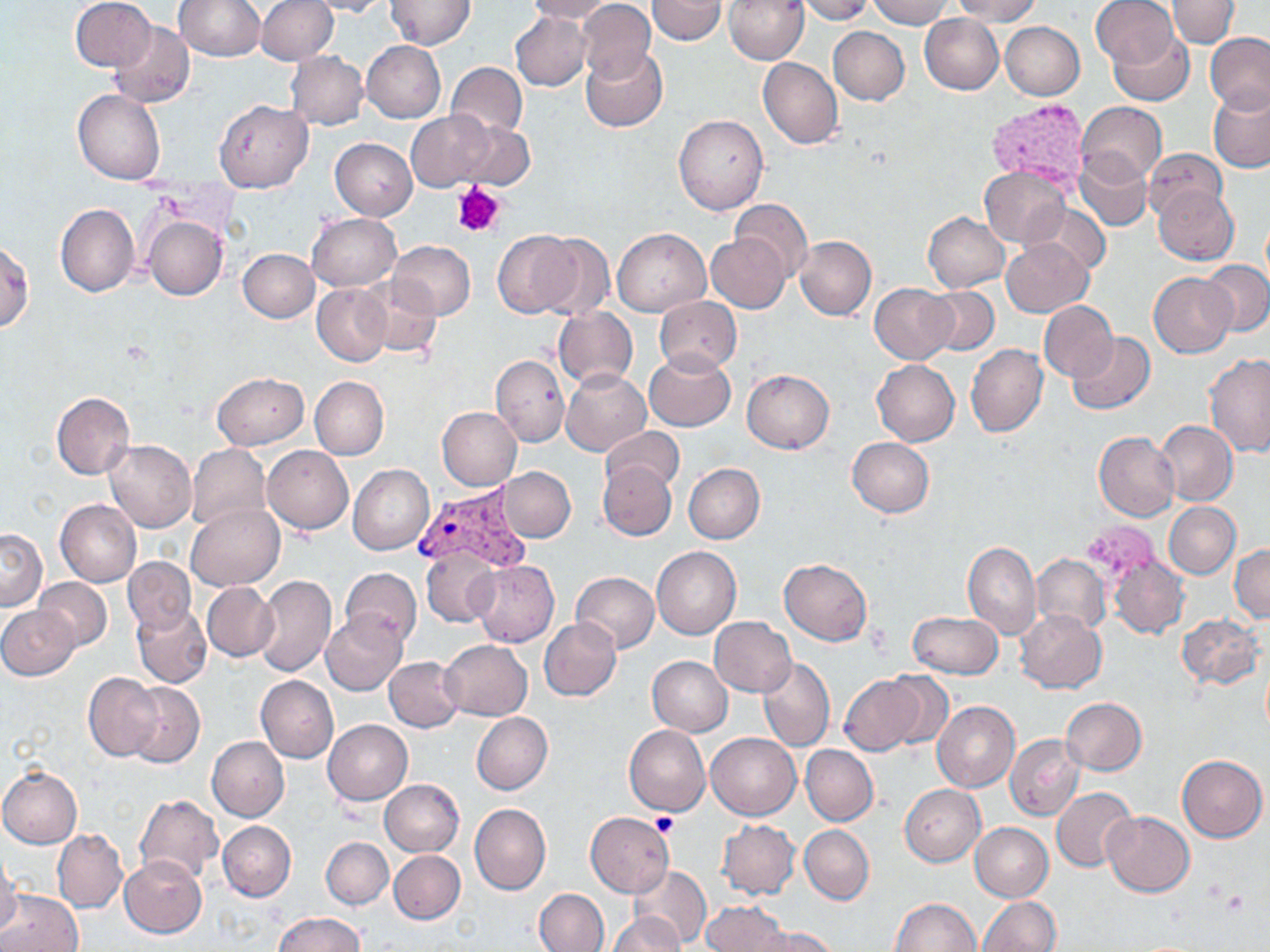

slide-level diagnosis = Plasmodium vivax
stain = May-Grünwald-Giemsa
modality = light microscopy
magnification = 1000x
image size = 1270×952 pixels
preparation = thin blood film
platelet locations = approximate bounding boxes as named x1/y1/x2/y2 corners in pixels: (x1=452, y1=181, x2=505, y2=239), (x1=651, y1=812, x2=676, y2=834)
uninfected red blood cell locations = approximate bounding boxes as named x1/y1/x2/y2 corners in pixels: (x1=71, y1=0, x2=157, y2=72), (x1=174, y1=0, x2=264, y2=61), (x1=256, y1=0, x2=338, y2=64), (x1=306, y1=0, x2=392, y2=17), (x1=385, y1=0, x2=476, y2=50), (x1=524, y1=0, x2=614, y2=23), (x1=576, y1=0, x2=655, y2=84), (x1=649, y1=0, x2=726, y2=46), (x1=796, y1=0, x2=874, y2=24), (x1=868, y1=0, x2=952, y2=26), (x1=950, y1=0, x2=1041, y2=25), (x1=1090, y1=0, x2=1180, y2=68), (x1=1167, y1=0, x2=1239, y2=48), (x1=723, y1=1, x2=808, y2=64), (x1=512, y1=13, x2=592, y2=90), (x1=919, y1=14, x2=1003, y2=94), (x1=108, y1=21, x2=195, y2=109), (x1=1001, y1=22, x2=1084, y2=99), (x1=828, y1=27, x2=909, y2=105), (x1=1107, y1=29, x2=1195, y2=107), (x1=1205, y1=32, x2=1270, y2=115), (x1=362, y1=40, x2=446, y2=123), (x1=581, y1=46, x2=667, y2=132), (x1=286, y1=52, x2=369, y2=129), (x1=757, y1=57, x2=842, y2=149), (x1=445, y1=61, x2=530, y2=140), (x1=72, y1=89, x2=166, y2=184), (x1=1208, y1=89, x2=1270, y2=172), (x1=214, y1=100, x2=313, y2=191), (x1=1076, y1=102, x2=1167, y2=186), (x1=405, y1=109, x2=501, y2=191), (x1=673, y1=113, x2=769, y2=215), (x1=451, y1=119, x2=537, y2=189), (x1=330, y1=138, x2=418, y2=220), (x1=321, y1=140, x2=408, y2=288), (x1=1144, y1=149, x2=1228, y2=223), (x1=1075, y1=152, x2=1151, y2=230), (x1=979, y1=166, x2=1071, y2=247), (x1=1154, y1=186, x2=1238, y2=264), (x1=731, y1=199, x2=812, y2=282), (x1=1027, y1=201, x2=1110, y2=276), (x1=56, y1=204, x2=139, y2=297), (x1=923, y1=212, x2=1010, y2=292), (x1=308, y1=213, x2=400, y2=290), (x1=142, y1=215, x2=228, y2=301), (x1=613, y1=228, x2=711, y2=315), (x1=494, y1=231, x2=583, y2=318), (x1=533, y1=232, x2=614, y2=321), (x1=706, y1=233, x2=789, y2=313), (x1=795, y1=236, x2=876, y2=320), (x1=1001, y1=239, x2=1094, y2=317), (x1=389, y1=240, x2=475, y2=319), (x1=0, y1=242, x2=33, y2=331), (x1=237, y1=249, x2=320, y2=321), (x1=1201, y1=259, x2=1270, y2=336), (x1=1149, y1=272, x2=1238, y2=357), (x1=356, y1=275, x2=444, y2=359), (x1=870, y1=283, x2=956, y2=364), (x1=312, y1=284, x2=392, y2=366), (x1=925, y1=287, x2=1001, y2=356), (x1=655, y1=296, x2=741, y2=373), (x1=1039, y1=301, x2=1118, y2=382), (x1=552, y1=306, x2=638, y2=390), (x1=1065, y1=332, x2=1155, y2=415), (x1=965, y1=344, x2=1047, y2=437), (x1=644, y1=351, x2=735, y2=431), (x1=490, y1=354, x2=569, y2=446), (x1=1203, y1=355, x2=1270, y2=457), (x1=872, y1=360, x2=960, y2=446), (x1=562, y1=369, x2=651, y2=455), (x1=741, y1=369, x2=835, y2=452), (x1=212, y1=372, x2=308, y2=449), (x1=309, y1=376, x2=388, y2=460), (x1=50, y1=391, x2=134, y2=480), (x1=437, y1=406, x2=522, y2=490), (x1=1156, y1=420, x2=1238, y2=507), (x1=600, y1=426, x2=685, y2=496), (x1=1094, y1=431, x2=1179, y2=521), (x1=846, y1=436, x2=934, y2=517), (x1=105, y1=439, x2=197, y2=533), (x1=186, y1=443, x2=270, y2=533), (x1=261, y1=445, x2=352, y2=534), (x1=598, y1=462, x2=677, y2=541), (x1=684, y1=463, x2=765, y2=543), (x1=348, y1=464, x2=433, y2=555), (x1=497, y1=467, x2=576, y2=542), (x1=56, y1=499, x2=140, y2=587), (x1=1164, y1=502, x2=1241, y2=578), (x1=185, y1=503, x2=283, y2=591), (x1=0, y1=528, x2=46, y2=611), (x1=962, y1=541, x2=1040, y2=638), (x1=1230, y1=544, x2=1270, y2=620), (x1=651, y1=547, x2=741, y2=639), (x1=421, y1=548, x2=499, y2=627), (x1=1031, y1=553, x2=1110, y2=634), (x1=123, y1=556, x2=197, y2=634), (x1=468, y1=559, x2=560, y2=647), (x1=779, y1=559, x2=872, y2=644), (x1=1109, y1=559, x2=1189, y2=639), (x1=339, y1=567, x2=421, y2=647), (x1=571, y1=573, x2=659, y2=654), (x1=252, y1=575, x2=337, y2=678), (x1=34, y1=577, x2=113, y2=651), (x1=202, y1=583, x2=278, y2=661), (x1=130, y1=603, x2=212, y2=688), (x1=0, y1=606, x2=79, y2=679), (x1=1015, y1=609, x2=1107, y2=693), (x1=321, y1=611, x2=408, y2=695), (x1=908, y1=611, x2=1003, y2=679), (x1=1177, y1=613, x2=1265, y2=690), (x1=709, y1=616, x2=796, y2=697), (x1=539, y1=619, x2=622, y2=700), (x1=439, y1=639, x2=532, y2=720), (x1=646, y1=655, x2=732, y2=736), (x1=758, y1=656, x2=834, y2=752), (x1=384, y1=657, x2=463, y2=732), (x1=84, y1=672, x2=160, y2=762), (x1=880, y1=672, x2=954, y2=750), (x1=255, y1=675, x2=338, y2=763), (x1=839, y1=675, x2=926, y2=754), (x1=123, y1=682, x2=205, y2=768), (x1=1061, y1=697, x2=1147, y2=774), (x1=932, y1=700, x2=1020, y2=793), (x1=471, y1=712, x2=552, y2=794), (x1=323, y1=719, x2=412, y2=804), (x1=623, y1=725, x2=710, y2=815), (x1=705, y1=731, x2=800, y2=820), (x1=1006, y1=735, x2=1084, y2=820), (x1=207, y1=736, x2=289, y2=822), (x1=800, y1=744, x2=878, y2=825), (x1=1177, y1=754, x2=1267, y2=842), (x1=0, y1=767, x2=82, y2=848), (x1=379, y1=779, x2=464, y2=856), (x1=899, y1=784, x2=985, y2=866), (x1=1051, y1=787, x2=1138, y2=872), (x1=135, y1=794, x2=223, y2=883), (x1=470, y1=804, x2=551, y2=895), (x1=1103, y1=811, x2=1195, y2=896), (x1=584, y1=813, x2=674, y2=897), (x1=717, y1=820, x2=800, y2=900), (x1=218, y1=821, x2=296, y2=901), (x1=970, y1=822, x2=1053, y2=902), (x1=800, y1=825, x2=874, y2=904), (x1=52, y1=828, x2=127, y2=913), (x1=321, y1=836, x2=393, y2=910), (x1=389, y1=850, x2=464, y2=923), (x1=0, y1=854, x2=22, y2=937), (x1=119, y1=856, x2=207, y2=938), (x1=633, y1=866, x2=712, y2=947), (x1=535, y1=888, x2=608, y2=952), (x1=1, y1=889, x2=84, y2=952), (x1=977, y1=896, x2=1060, y2=951), (x1=888, y1=898, x2=981, y2=952), (x1=702, y1=900, x2=791, y2=952), (x1=276, y1=913, x2=364, y2=951), (x1=609, y1=913, x2=683, y2=952), (x1=752, y1=924, x2=841, y2=952)
Plasmodium vivax-infected red blood cell locations = approximate bounding boxes as named x1/y1/x2/y2 corners in pixels: (x1=415, y1=484, x2=527, y2=572)
field of view = single